Locate every uninfected red blood cell.
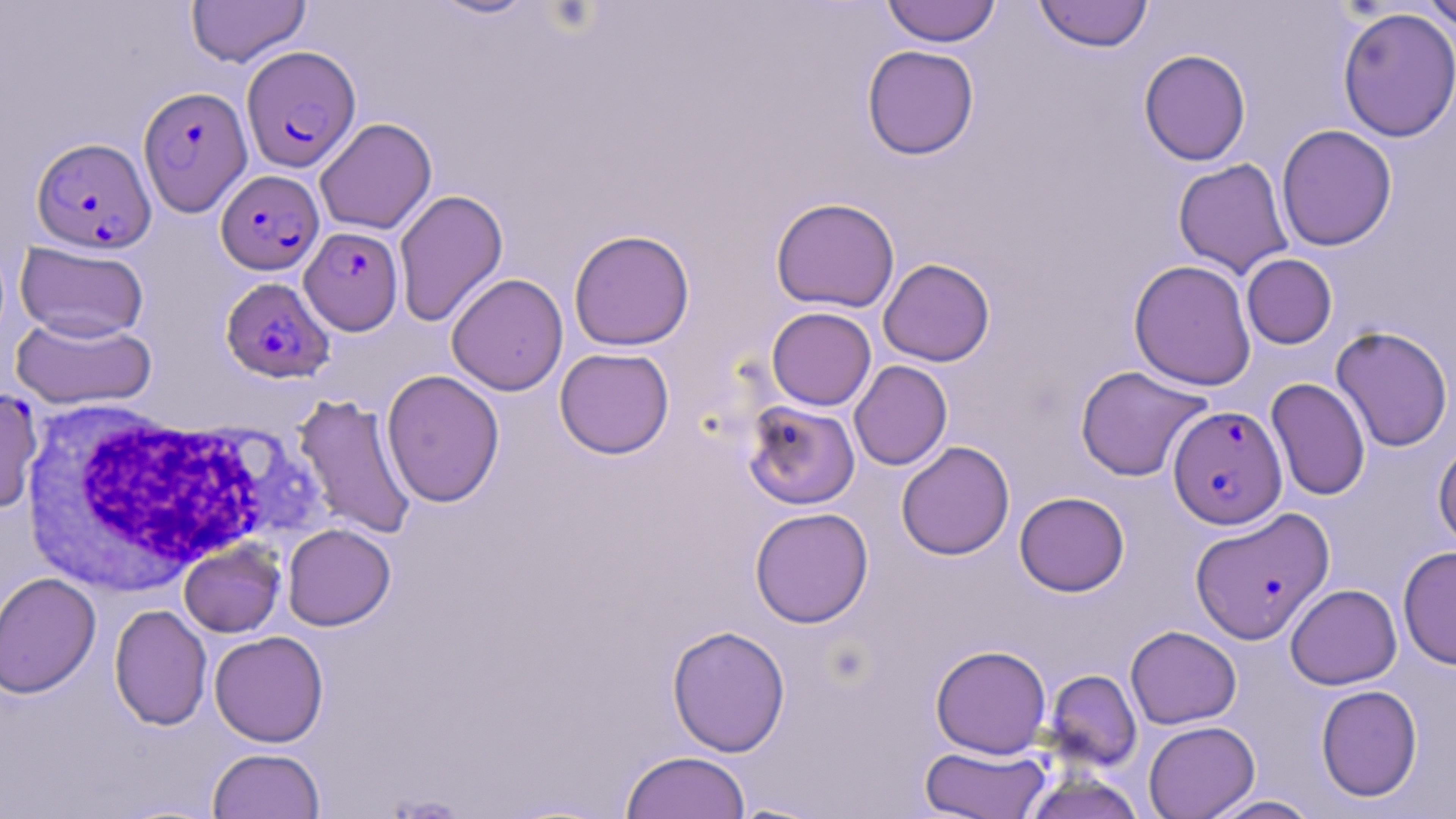
Approximate bounding boxes as (x1, y1, x2, y2) in pixels.
Uninfected red blood cells: (186, 0, 311, 67), (425, 0, 542, 20), (881, 0, 1000, 47), (1034, 0, 1153, 52), (1419, 0, 1456, 33), (1337, 7, 1455, 143), (861, 45, 979, 159), (1138, 49, 1251, 166), (315, 118, 437, 235), (1276, 124, 1397, 251), (1173, 158, 1293, 278), (393, 189, 508, 328), (770, 197, 900, 313), (568, 229, 695, 351), (15, 241, 150, 342), (1241, 254, 1337, 349), (878, 258, 995, 366), (1128, 259, 1256, 391), (446, 273, 569, 396), (767, 307, 876, 411), (10, 315, 156, 410), (1330, 325, 1454, 452), (554, 347, 675, 459), (849, 360, 952, 470), (1075, 365, 1211, 482), (381, 369, 505, 507), (1266, 378, 1370, 501), (293, 393, 418, 540), (743, 400, 860, 510), (1433, 440, 1456, 550), (896, 441, 1015, 560), (1014, 491, 1129, 596), (750, 506, 874, 628), (282, 524, 395, 630), (179, 541, 285, 638), (1398, 545, 1455, 670), (0, 571, 102, 699), (1285, 584, 1402, 689), (109, 604, 212, 730), (666, 625, 790, 756), (1125, 625, 1241, 729), (209, 630, 328, 747), (930, 644, 1051, 758), (1043, 669, 1142, 772), (1315, 684, 1422, 802), (1143, 720, 1260, 819), (920, 744, 1051, 819), (207, 747, 326, 819), (620, 750, 751, 819), (1020, 771, 1147, 819), (1202, 795, 1322, 818), (725, 801, 831, 818).

slide-level diagnosis = Plasmodium falciparum
magnification = 1000x
preparation = thin blood film
field of view = single
image size = 1456×819 pixels
white blood cell locations = approximate bounding boxes as (x1, y1, x2, y2) in pixels: (19, 398, 279, 598)
modality = light microscopy
stain = May-Grünwald-Giemsa
Plasmodium falciparum-infected red blood cell locations = approximate bounding boxes as (x1, y1, x2, y2) in pixels: (242, 45, 361, 172), (138, 85, 252, 217), (31, 136, 156, 254), (215, 170, 324, 275), (300, 226, 403, 335), (220, 277, 334, 383), (0, 387, 43, 515), (1169, 405, 1286, 528), (1188, 507, 1333, 644)